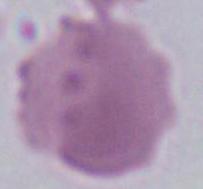 Photomicrograph. An erythrocyte is shown. Captured at 1000x magnification.